State which parasite is depicted.
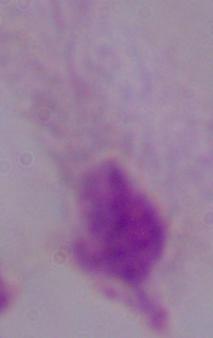

This is a trichomonad.

Summary:
  - Magnification: 1000x
  - Modality: photomicrograph